Point out each Plasmodium parasite.
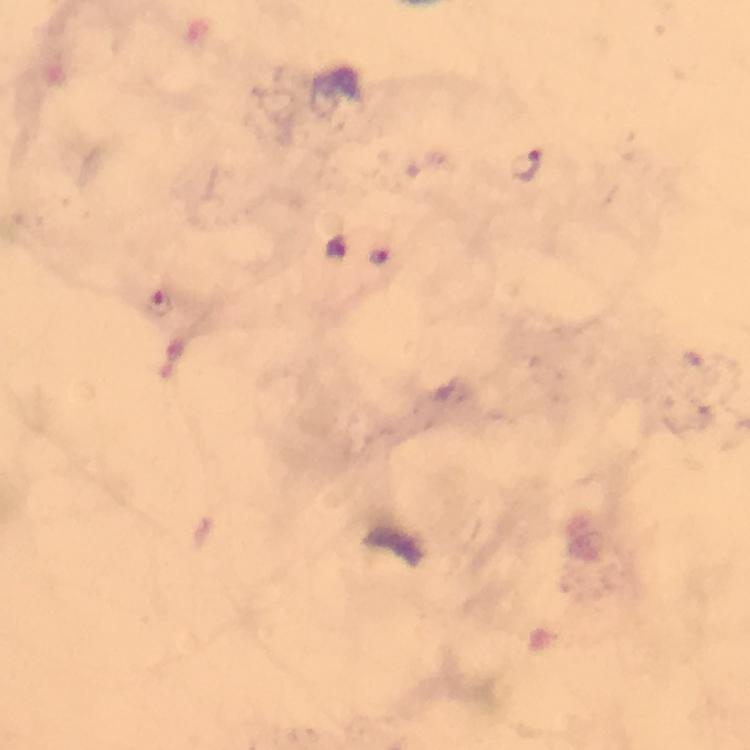

Approximate centers as [x, y] in pixels.
Plasmodium parasites: [527, 163], [335, 248], [377, 255], [158, 300].

stain = Giemsa
preparation = thick blood film
image size = 750×750 pixels
context = from a diagnostic examination for malaria
cropped from = a single field of view
capture = smartphone mounted on the microscope
immersion oil = applied
magnification = 100x